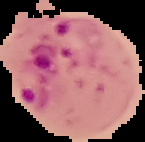

Image is 145×142 pixels. Malaria status: parasitized. The area outside the segmented cell region is set to black. From a thin blood film.